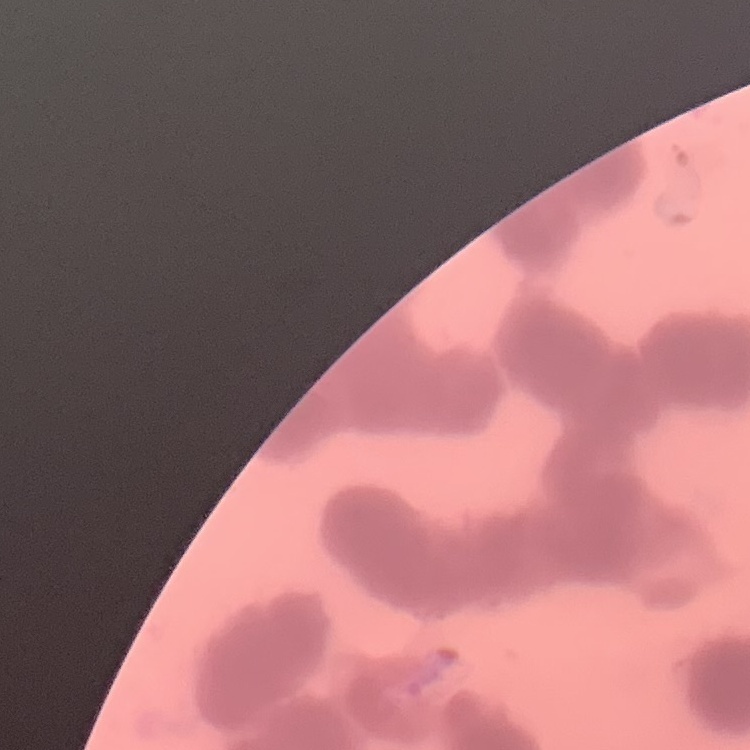
Summary:
  - Erythrocyte morphology: rouleaux formation
  - Image type: one tile cut from a larger photomicrograph
  - Stain: Field's or Giemsa
  - Preparation: thin blood film